Point out each malaria parasite.
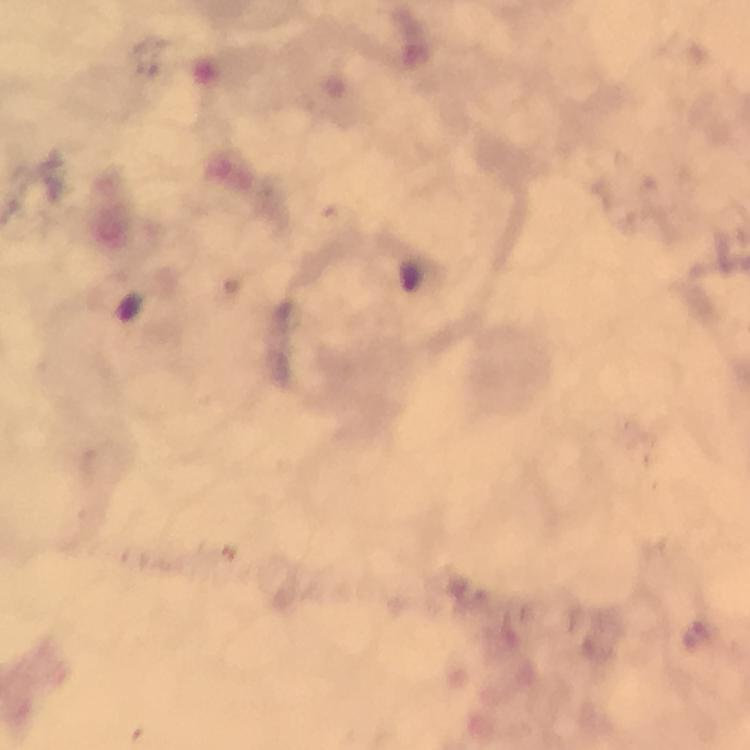
Approximate centers as [x, y] in pixels.
Malaria parasites: [693, 635].

preparation = thick blood film
capture = smartphone camera through the microscope
magnification = 100x
context = from a diagnostic examination for malaria
stain = Giemsa
immersion oil = applied
cropped from = a single field of view
image size = 750×750 pixels